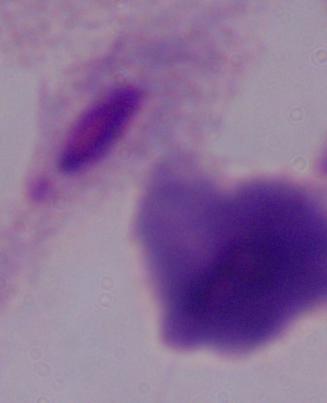 1000x magnification. A trichomonad is seen. Micrograph.